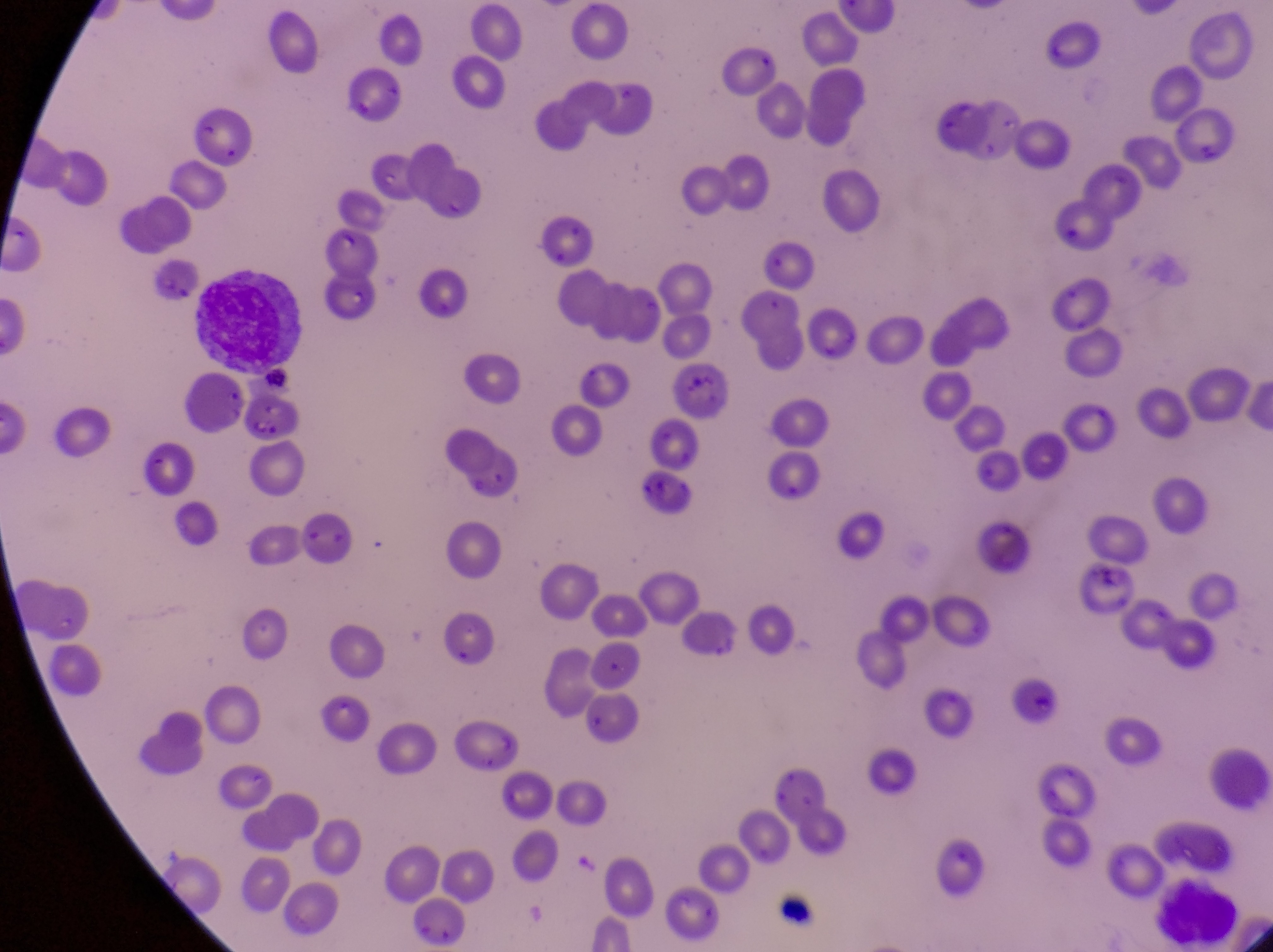 Approximate bounding boxes as [left, top, right, bottom] in pixels. Leukocyte locations: [188, 275, 303, 372], [1160, 876, 1244, 932]. Artifact (platelet-like body, stain precipitate, or debris) locations: [671, 367, 729, 415], [646, 470, 694, 510], [1078, 557, 1135, 592], [1011, 682, 1058, 724]. Image is 1273×952 pixels. At a magnification of 1000x. Photographed through the eyepiece of an Olympus CX-23 microscope with a smartphone camera. Sample from Uganda. One field of view. Thin blood film.